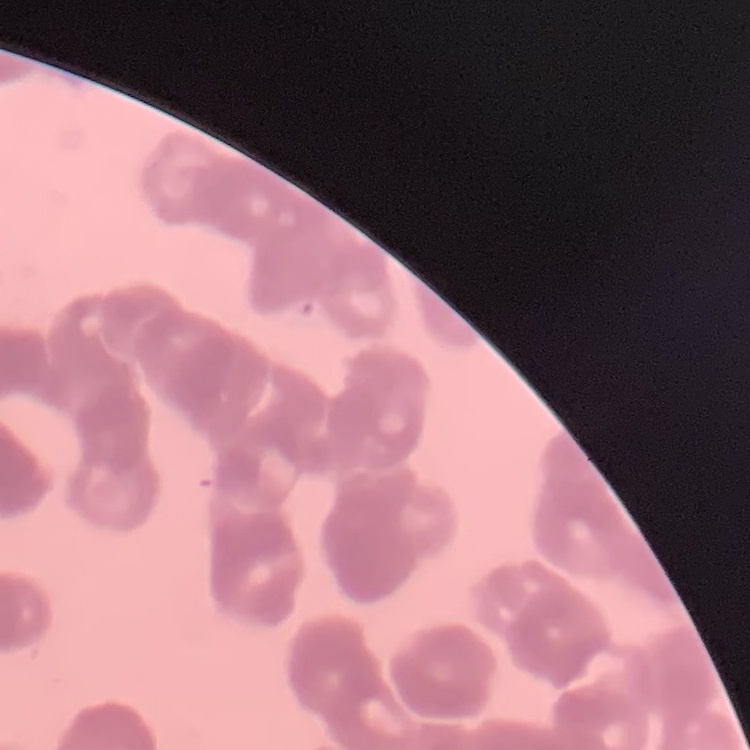

Summary:
  - Erythrocyte morphology: rouleaux formation
  - Preparation: thin peripheral smear
  - Stain: Field's or Giemsa
  - Image type: one tile cut from a larger photomicrograph